Classify this cell by malaria status.
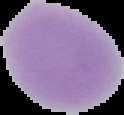

It is uninfected.

From a thin blood film. Image is 124×115 pixels. Segmented cell region on a black background.